Describe the morphology of the red blood cells.
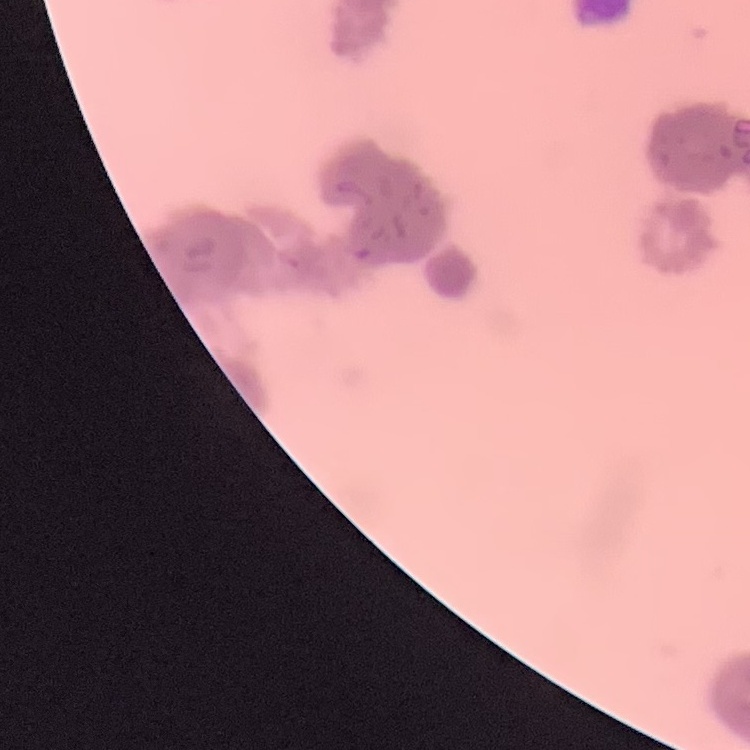

Rouleaux formation.

preparation: thin peripheral smear
image_type: square crop of a larger photomicrograph
stain: Field's or Giemsa